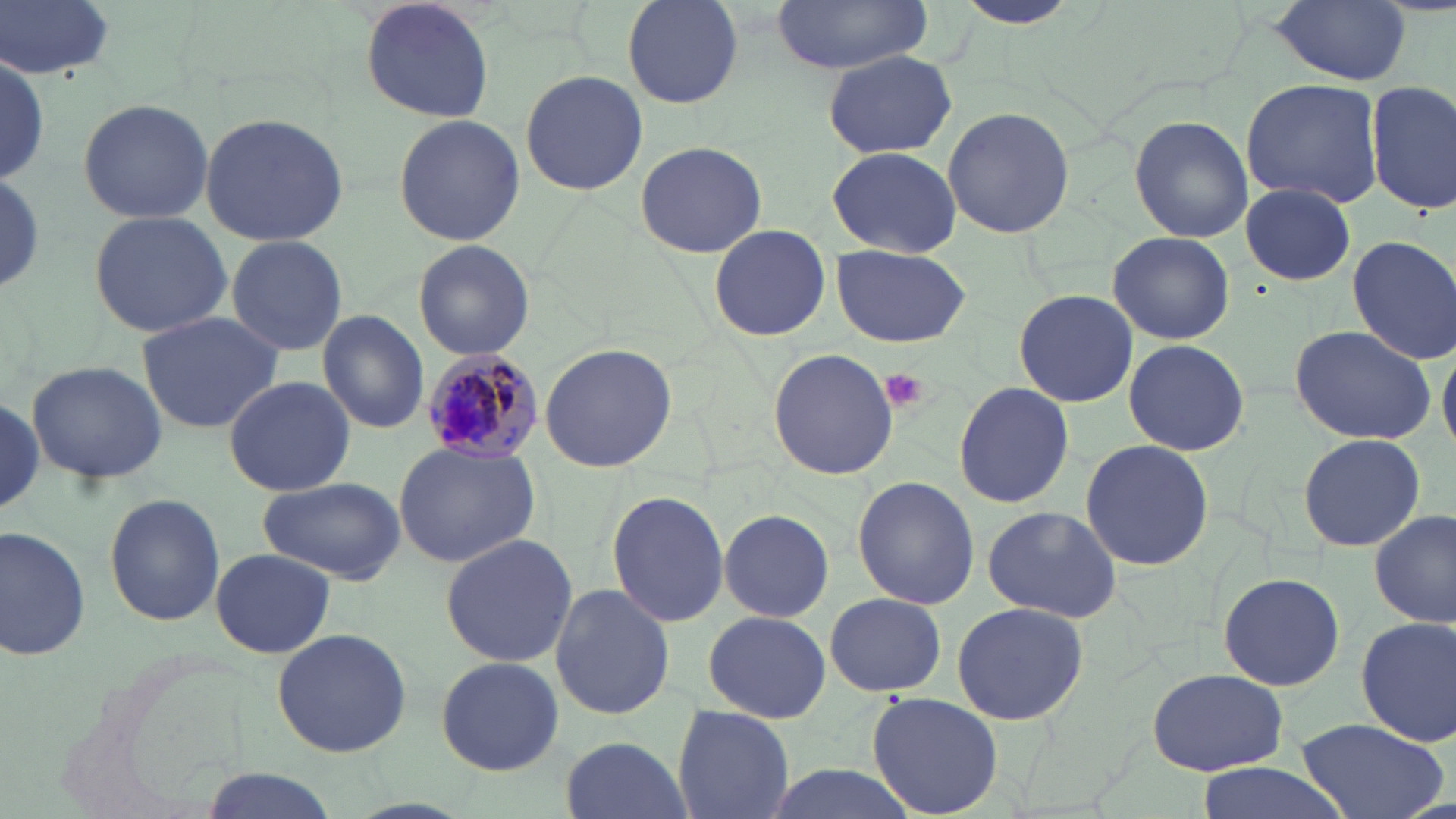

Summary:
  - Coordinate format: approximate bounding boxes as (x1, y1, x2, y2) in pixels
  - Uninfected red blood cell locations: (0, 0, 119, 78), (361, 0, 493, 125), (624, 0, 744, 108), (945, 0, 1089, 32), (1264, 0, 1416, 84), (769, 1, 936, 73), (824, 51, 956, 158), (1, 53, 51, 190), (520, 68, 648, 195), (1240, 78, 1385, 210), (1365, 80, 1455, 214), (77, 97, 214, 224), (941, 104, 1077, 240), (199, 110, 353, 248), (392, 113, 525, 248), (1129, 115, 1253, 243), (633, 140, 768, 259), (828, 142, 964, 257), (1241, 184, 1358, 285), (86, 210, 233, 337), (707, 223, 831, 342), (1107, 231, 1234, 346), (222, 236, 348, 356), (1347, 236, 1456, 362), (410, 241, 535, 360), (830, 245, 969, 349), (1012, 288, 1138, 408), (133, 309, 285, 433), (317, 309, 430, 434), (1287, 323, 1436, 445), (1123, 338, 1251, 456), (1439, 340, 1456, 454), (538, 341, 680, 473), (768, 348, 899, 481), (25, 358, 169, 486), (225, 374, 355, 496), (953, 382, 1073, 508), (1297, 432, 1426, 552), (1080, 439, 1212, 573), (393, 440, 542, 569), (258, 476, 407, 585), (852, 476, 980, 611), (605, 489, 729, 627), (104, 492, 226, 627), (982, 503, 1123, 622), (1371, 507, 1454, 630), (717, 509, 834, 620), (0, 523, 91, 661), (439, 534, 580, 670), (209, 548, 335, 658), (1216, 572, 1346, 692), (550, 583, 674, 721), (822, 592, 947, 696), (950, 602, 1094, 726), (701, 611, 831, 722), (1355, 614, 1456, 750), (271, 627, 412, 758), (433, 654, 564, 775), (1148, 668, 1288, 776), (866, 691, 1002, 817), (672, 704, 795, 819), (1295, 717, 1447, 819), (560, 734, 689, 819), (1189, 760, 1353, 819), (762, 764, 921, 819), (196, 770, 339, 819)
  - Platelet locations: (880, 368, 929, 412)
  - Plasmodium malariae-infected red blood cell locations: (421, 349, 544, 465)
  - Slide-level diagnosis: Plasmodium malariae
  - Modality: optical microscopy
  - Image size: 1456×819 pixels
  - Preparation: thin blood smear
  - Magnification: 1000x
  - Field of view: one of a larger specimen
  - Stain: May-Grünwald-Giemsa